Assess this cell for malaria.
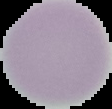

It is uninfected.

image size = 112×109 pixels
image type = cell region segmented out of the field of view; surrounding area masked to black
preparation = thin blood film